Locate every leukocyte (white blood cell).
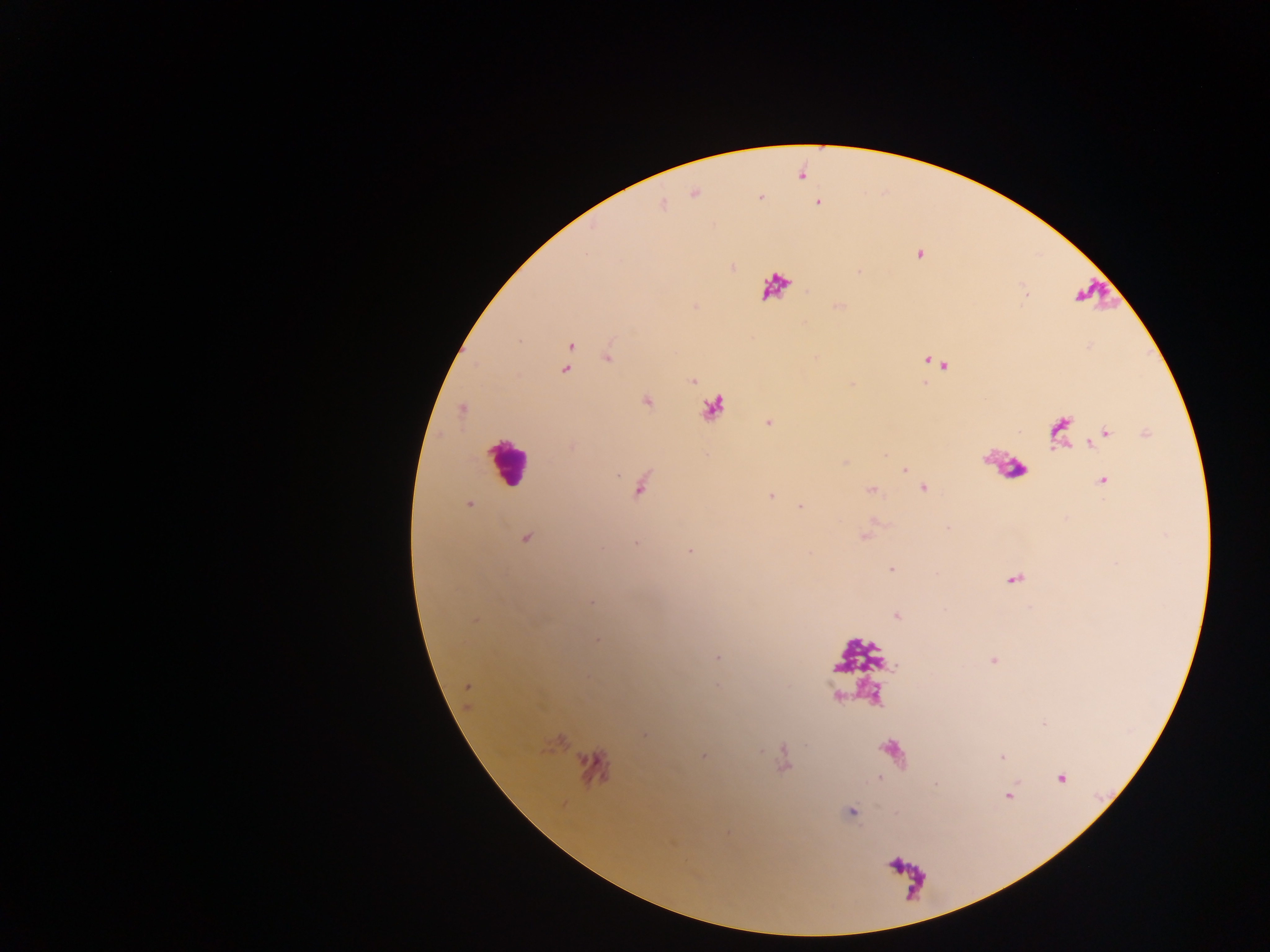

Approximate centers as {x, y} in pixels.
Leukocytes: {774, 287}, {1098, 296}, {714, 408}, {508, 463}, {1006, 465}, {857, 656}, {862, 694}, {894, 755}, {595, 769}, {907, 877}.
One object is labeled both malaria parasite and leukocyte by the source: {1060, 431}.

Malaria parasite locations: {695, 192}, {760, 197}, {817, 202}, {662, 204}, {918, 255}, {732, 266}, {859, 271}, {837, 307}, {569, 345}, {607, 356}, {932, 362}, {942, 365}, {565, 369}, {693, 381}, {852, 383}, {925, 383}, {646, 401}, {462, 408}, {768, 422}, {1105, 433}, {1146, 433}, {882, 454}, {844, 461}, {905, 470}, {1102, 480}, {640, 484}, {923, 488}, {871, 489}, {770, 495}, {469, 503}, {800, 506}, {863, 535}, {525, 538}, {636, 543}, {690, 550}, {891, 568}, {1014, 578}, {591, 601}, {896, 616}, {597, 640}, {716, 656}, {994, 660}, {467, 686}, {717, 687}, {1042, 724}, {644, 734}, {702, 755}, {1002, 756}, {1061, 777}, {1008, 795}, {851, 811}. Mobile-phone photograph taken through the microscope. Image is 1270×952 pixels. Thick blood film. Sample from Ghana. One field of view.